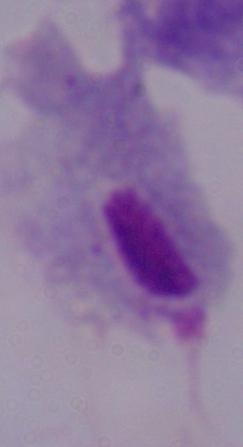
Summary:
  - Modality: photomicrograph
  - Identification: trichomonad
  - Magnification: 1000x